Outline each blood parasite and name the species.
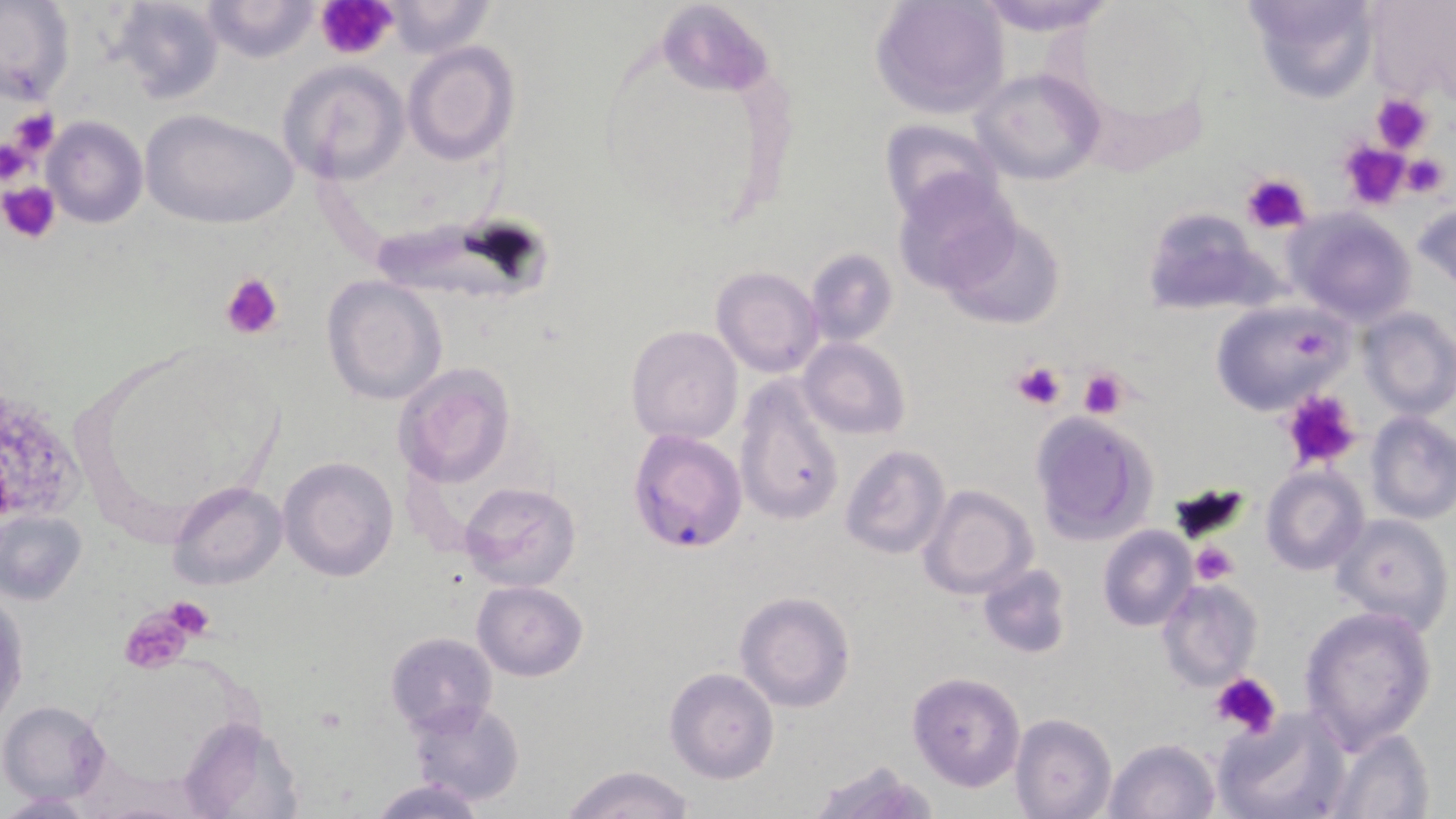

Approximate bounding boxes as [x1, y1, x2, y2] in pixels.
Plasmodium falciparum-infected red blood cells: [627, 427, 748, 555].
No Plasmodium ovale, Plasmodium malariae, Plasmodium vivax, Babesia divergens, or Trypanosoma brucei observed.

slide-level diagnosis = Plasmodium falciparum
modality = optical microscopy
field of view = one of a larger specimen
stain = May-Grünwald-Giemsa
preparation = thin blood smear
uninfected red blood cell locations = approximate bounding boxes as [x1, y1, x2, y2] in pixels: [110, 0, 227, 104], [199, 0, 325, 63], [870, 0, 1010, 119], [976, 0, 1114, 33], [1247, 0, 1381, 104], [1364, 0, 1456, 106], [0, 1, 75, 103], [383, 2, 498, 58], [660, 16, 770, 96], [404, 43, 519, 165], [280, 63, 405, 185], [973, 67, 1104, 185], [138, 106, 298, 229], [43, 116, 147, 229], [876, 116, 1005, 222], [892, 171, 1022, 297], [1413, 201, 1456, 292], [1141, 208, 1275, 317], [1287, 210, 1416, 325], [361, 214, 555, 309], [943, 215, 1067, 331], [805, 249, 898, 346], [711, 267, 823, 378], [323, 276, 448, 406], [1208, 302, 1347, 414], [1358, 308, 1456, 418], [625, 324, 743, 445], [798, 337, 912, 439], [393, 363, 514, 489], [733, 376, 845, 527], [1367, 412, 1456, 524], [1030, 413, 1156, 544], [839, 445, 950, 560], [277, 455, 399, 583], [1262, 466, 1368, 577], [169, 480, 286, 588], [459, 480, 581, 590], [917, 484, 1039, 601], [1, 510, 86, 607], [1332, 513, 1453, 634], [1098, 524, 1198, 632], [977, 563, 1071, 661], [1156, 579, 1262, 689], [473, 581, 588, 679], [734, 591, 855, 712], [1, 593, 28, 727], [1300, 605, 1438, 752], [385, 632, 498, 737], [664, 666, 779, 783], [908, 672, 1028, 792], [410, 700, 527, 805], [1, 701, 111, 805], [1216, 709, 1351, 819], [1010, 711, 1117, 818], [177, 714, 304, 816], [1320, 725, 1435, 819], [1102, 738, 1221, 819], [805, 758, 942, 819], [560, 764, 696, 819], [367, 777, 488, 819]
magnification = 1000x
image size = 1456×819 pixels
platelet locations = approximate bounding boxes as [x1, y1, x2, y2] in pixels: [314, 0, 397, 58], [1371, 93, 1434, 153], [3, 104, 61, 168], [0, 136, 32, 189], [1336, 142, 1413, 210], [1400, 153, 1450, 198], [1242, 172, 1313, 234], [0, 180, 61, 245], [220, 272, 284, 341], [1011, 359, 1068, 410], [1077, 368, 1128, 417], [1278, 388, 1364, 472], [1169, 486, 1247, 544], [1189, 542, 1238, 584], [162, 596, 216, 642], [119, 604, 201, 674], [1209, 672, 1282, 741]